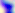

Summary:
  - Identification: Toxoplasma gondii
  - Magnification: 400x
  - Modality: micrograph